Classify this cell by malaria status.
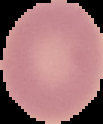

Uninfected.

The area outside the segmented cell region is set to black. Image is 103×124 pixels. From a thin blood film.